Report the malaria status of this cell.
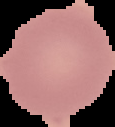

It is uninfected.

Summary:
  - Image type: segmented cell region on a black background
  - Image size: 115×127 pixels
  - Preparation: thin blood film